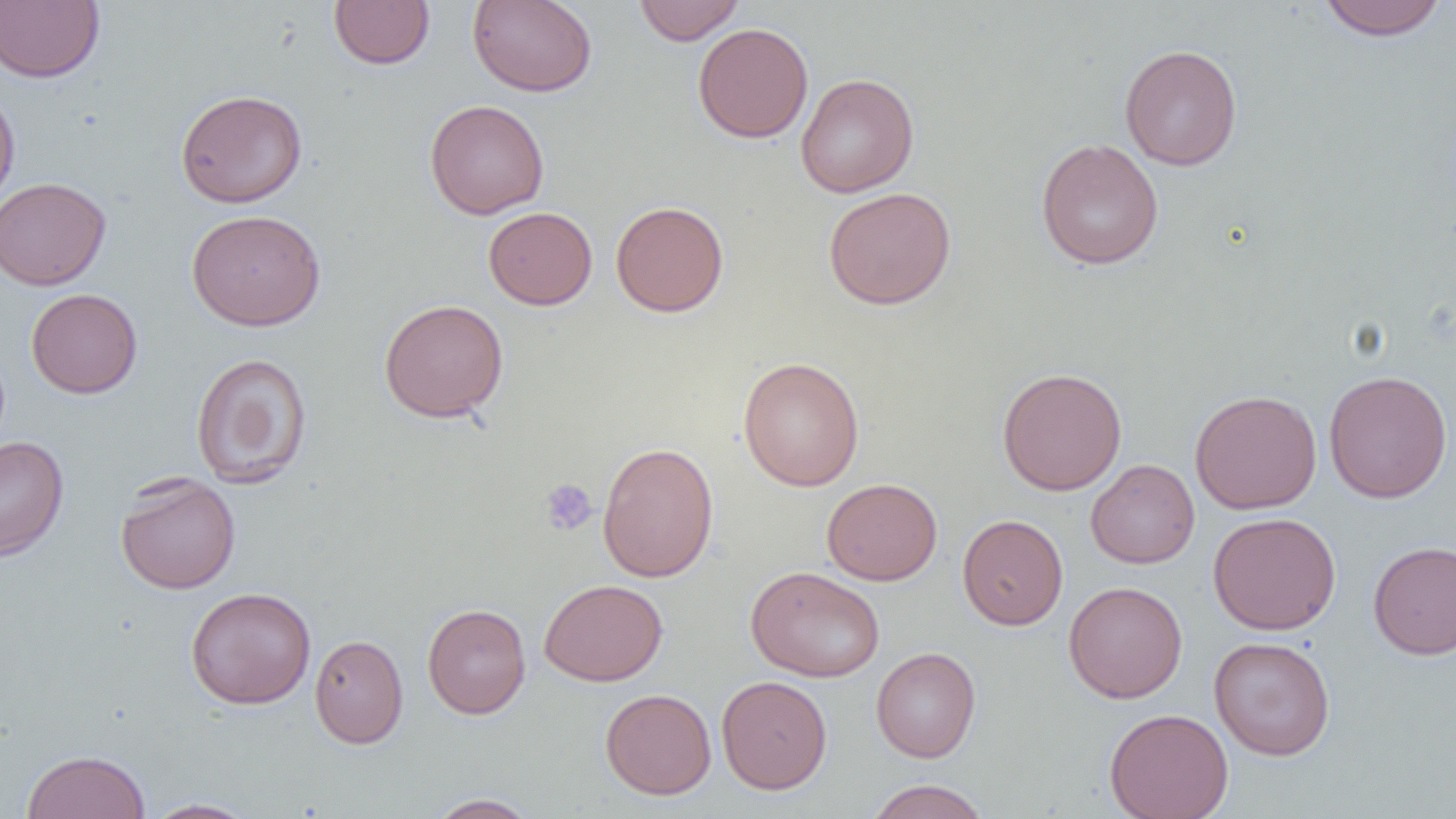

slide-level diagnosis = negative for blood parasites
preparation = thin blood film
field of view = single
magnification = 1000x
uninfected red blood cell locations = approximate bounding boxes as [x1, y1, x2, y2] in pixels: [328, 0, 435, 69], [467, 0, 597, 97], [633, 0, 745, 46], [1317, 0, 1448, 40], [0, 1, 105, 84], [692, 22, 814, 143], [1120, 43, 1242, 170], [795, 73, 919, 198], [0, 87, 20, 213], [175, 88, 308, 208], [424, 99, 549, 219], [1036, 138, 1164, 269], [0, 177, 111, 290], [823, 186, 957, 310], [610, 201, 729, 317], [483, 206, 598, 310], [187, 209, 326, 331], [26, 289, 143, 398], [379, 298, 509, 422], [191, 352, 312, 489], [737, 356, 865, 491], [997, 367, 1127, 495], [1323, 370, 1453, 504], [1189, 389, 1322, 514], [0, 436, 69, 561], [597, 442, 719, 582], [1086, 459, 1200, 569], [114, 473, 241, 595], [822, 477, 943, 585], [1208, 512, 1341, 635], [957, 514, 1068, 630], [1368, 539, 1456, 660], [746, 566, 885, 683], [538, 579, 668, 686], [1063, 581, 1187, 703], [185, 586, 317, 709], [422, 603, 531, 719], [309, 634, 409, 748], [1209, 636, 1335, 760], [871, 647, 981, 762], [716, 675, 832, 794], [600, 688, 717, 800], [1104, 708, 1234, 819], [21, 749, 151, 819], [864, 779, 991, 819], [425, 793, 540, 818], [142, 798, 259, 818]
platelet locations = approximate bounding boxes as [x1, y1, x2, y2] in pixels: [539, 478, 599, 536]
modality = optical microscopy
image size = 1456×819 pixels